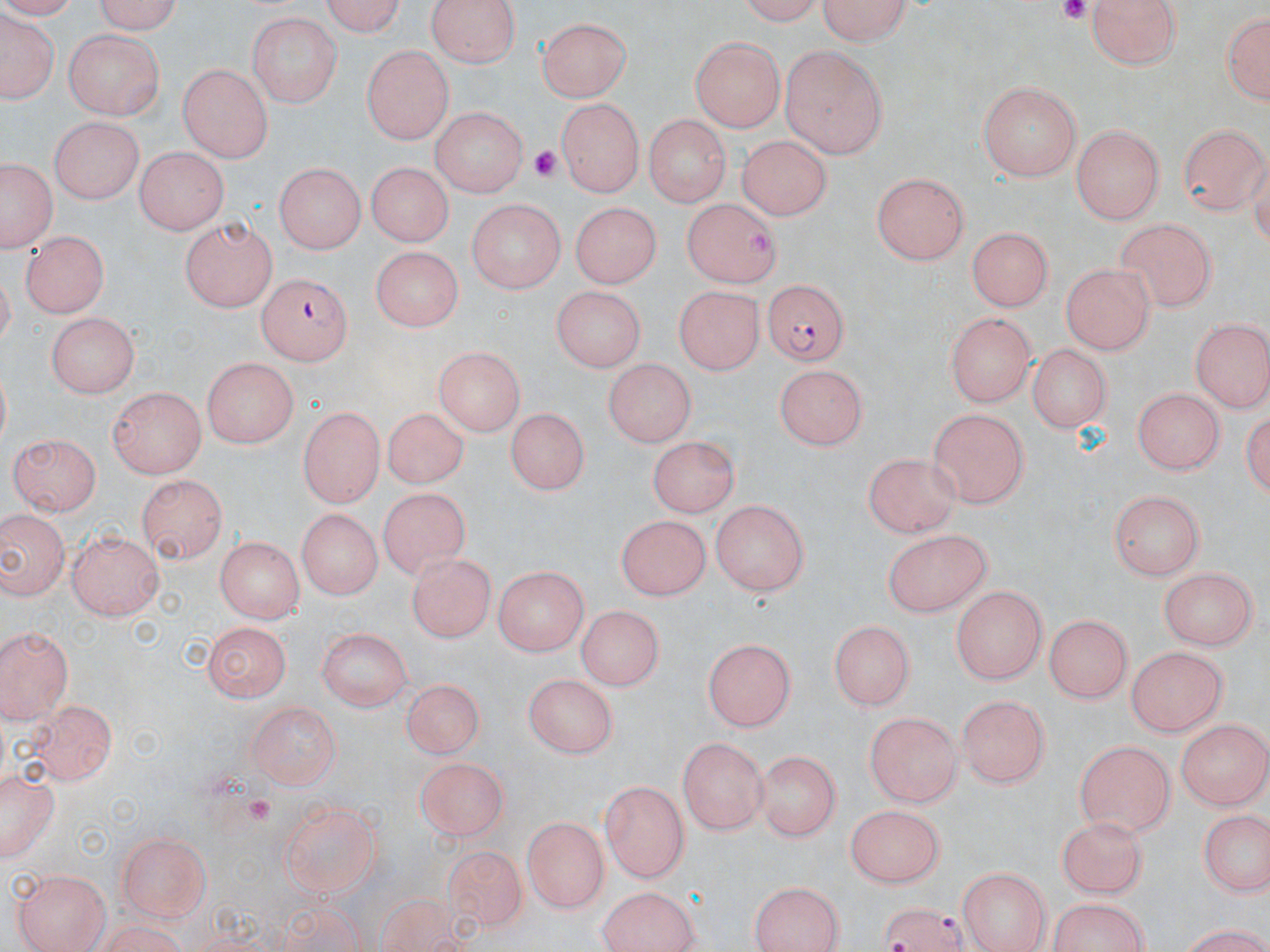
slide_level_diagnosis: Plasmodium falciparum
magnification: 1000x
stain: May-Grünwald-Giemsa
preparation: thin blood film
plasmodium_falciparum_infected_red_blood_cell_locations: 'approximate bounding boxes as named x1/y1/x2/y2 corners in pixels: (x1=258, y1=272, x2=355, y2=362), (x1=765, y1=280, x2=849, y2=368), (x1=873, y1=900, x2=973, y2=951)'
image_size: 1270×952 pixels
field_of_view: one of a larger specimen
modality: light microscopy
platelet_locations: 'approximate bounding boxes as named x1/y1/x2/y2 corners in pixels: (x1=1050, y1=0, x2=1097, y2=23), (x1=531, y1=144, x2=569, y2=181), (x1=241, y1=795, x2=281, y2=829)'
uninfected_red_blood_cell_locations: 'approximate bounding boxes as named x1/y1/x2/y2 corners in pixels: (x1=86, y1=0, x2=183, y2=32), (x1=314, y1=0, x2=405, y2=34), (x1=422, y1=0, x2=522, y2=68), (x1=812, y1=0, x2=918, y2=44), (x1=1084, y1=0, x2=1182, y2=71), (x1=733, y1=1, x2=828, y2=22), (x1=1217, y1=5, x2=1268, y2=112), (x1=246, y1=12, x2=340, y2=108), (x1=2, y1=14, x2=55, y2=106), (x1=539, y1=16, x2=631, y2=103), (x1=64, y1=30, x2=166, y2=118), (x1=689, y1=37, x2=783, y2=132), (x1=361, y1=43, x2=454, y2=144), (x1=778, y1=43, x2=887, y2=159), (x1=176, y1=65, x2=275, y2=162), (x1=978, y1=80, x2=1082, y2=182), (x1=554, y1=98, x2=645, y2=195), (x1=429, y1=106, x2=529, y2=198), (x1=641, y1=114, x2=730, y2=204), (x1=48, y1=116, x2=143, y2=204), (x1=1178, y1=124, x2=1267, y2=215), (x1=1070, y1=128, x2=1163, y2=223), (x1=736, y1=135, x2=834, y2=217), (x1=133, y1=146, x2=229, y2=233), (x1=1, y1=154, x2=57, y2=254), (x1=365, y1=159, x2=451, y2=249), (x1=273, y1=162, x2=364, y2=255), (x1=870, y1=170, x2=973, y2=265), (x1=678, y1=197, x2=781, y2=287), (x1=466, y1=199, x2=563, y2=295), (x1=569, y1=200, x2=665, y2=291), (x1=180, y1=216, x2=274, y2=314), (x1=1113, y1=216, x2=1218, y2=312), (x1=964, y1=227, x2=1052, y2=312), (x1=19, y1=230, x2=110, y2=318), (x1=367, y1=247, x2=464, y2=331), (x1=1061, y1=261, x2=1158, y2=352), (x1=673, y1=285, x2=765, y2=375), (x1=551, y1=286, x2=644, y2=375), (x1=46, y1=312, x2=140, y2=396), (x1=946, y1=313, x2=1033, y2=409), (x1=1189, y1=320, x2=1268, y2=412), (x1=1025, y1=342, x2=1112, y2=433), (x1=433, y1=345, x2=526, y2=435), (x1=202, y1=356, x2=300, y2=445), (x1=602, y1=359, x2=699, y2=447), (x1=774, y1=363, x2=872, y2=448), (x1=106, y1=387, x2=207, y2=477), (x1=1130, y1=388, x2=1222, y2=478), (x1=297, y1=403, x2=384, y2=510), (x1=505, y1=406, x2=588, y2=498), (x1=926, y1=406, x2=1029, y2=507), (x1=381, y1=408, x2=469, y2=489), (x1=8, y1=431, x2=101, y2=516), (x1=645, y1=435, x2=742, y2=515), (x1=860, y1=449, x2=963, y2=533), (x1=129, y1=478, x2=223, y2=559), (x1=378, y1=485, x2=466, y2=573), (x1=1108, y1=490, x2=1203, y2=581), (x1=711, y1=499, x2=812, y2=600), (x1=294, y1=508, x2=384, y2=600), (x1=0, y1=510, x2=68, y2=602), (x1=615, y1=512, x2=709, y2=599), (x1=884, y1=526, x2=996, y2=617), (x1=68, y1=528, x2=167, y2=623), (x1=214, y1=533, x2=304, y2=620), (x1=406, y1=550, x2=495, y2=641), (x1=494, y1=565, x2=589, y2=655), (x1=1159, y1=567, x2=1258, y2=650), (x1=952, y1=585, x2=1048, y2=683), (x1=577, y1=607, x2=660, y2=692), (x1=1042, y1=613, x2=1134, y2=703), (x1=831, y1=618, x2=918, y2=708), (x1=201, y1=620, x2=292, y2=700), (x1=0, y1=623, x2=76, y2=722), (x1=318, y1=626, x2=412, y2=712), (x1=703, y1=636, x2=799, y2=734), (x1=1125, y1=644, x2=1229, y2=738), (x1=524, y1=672, x2=619, y2=756), (x1=396, y1=680, x2=481, y2=757), (x1=957, y1=692, x2=1052, y2=790), (x1=19, y1=699, x2=119, y2=787), (x1=243, y1=700, x2=344, y2=787), (x1=865, y1=709, x2=963, y2=806), (x1=1178, y1=718, x2=1269, y2=810), (x1=679, y1=737, x2=769, y2=833), (x1=1074, y1=740, x2=1174, y2=838), (x1=757, y1=747, x2=841, y2=843), (x1=418, y1=762, x2=507, y2=838), (x1=1, y1=769, x2=58, y2=864), (x1=601, y1=779, x2=690, y2=884), (x1=280, y1=800, x2=382, y2=899), (x1=843, y1=803, x2=944, y2=888), (x1=1199, y1=809, x2=1268, y2=898), (x1=523, y1=816, x2=607, y2=914), (x1=1055, y1=816, x2=1146, y2=897), (x1=113, y1=830, x2=214, y2=921), (x1=443, y1=843, x2=524, y2=934), (x1=957, y1=867, x2=1051, y2=952), (x1=14, y1=868, x2=110, y2=952), (x1=747, y1=879, x2=849, y2=951), (x1=596, y1=886, x2=702, y2=952), (x1=1045, y1=895, x2=1152, y2=952)'